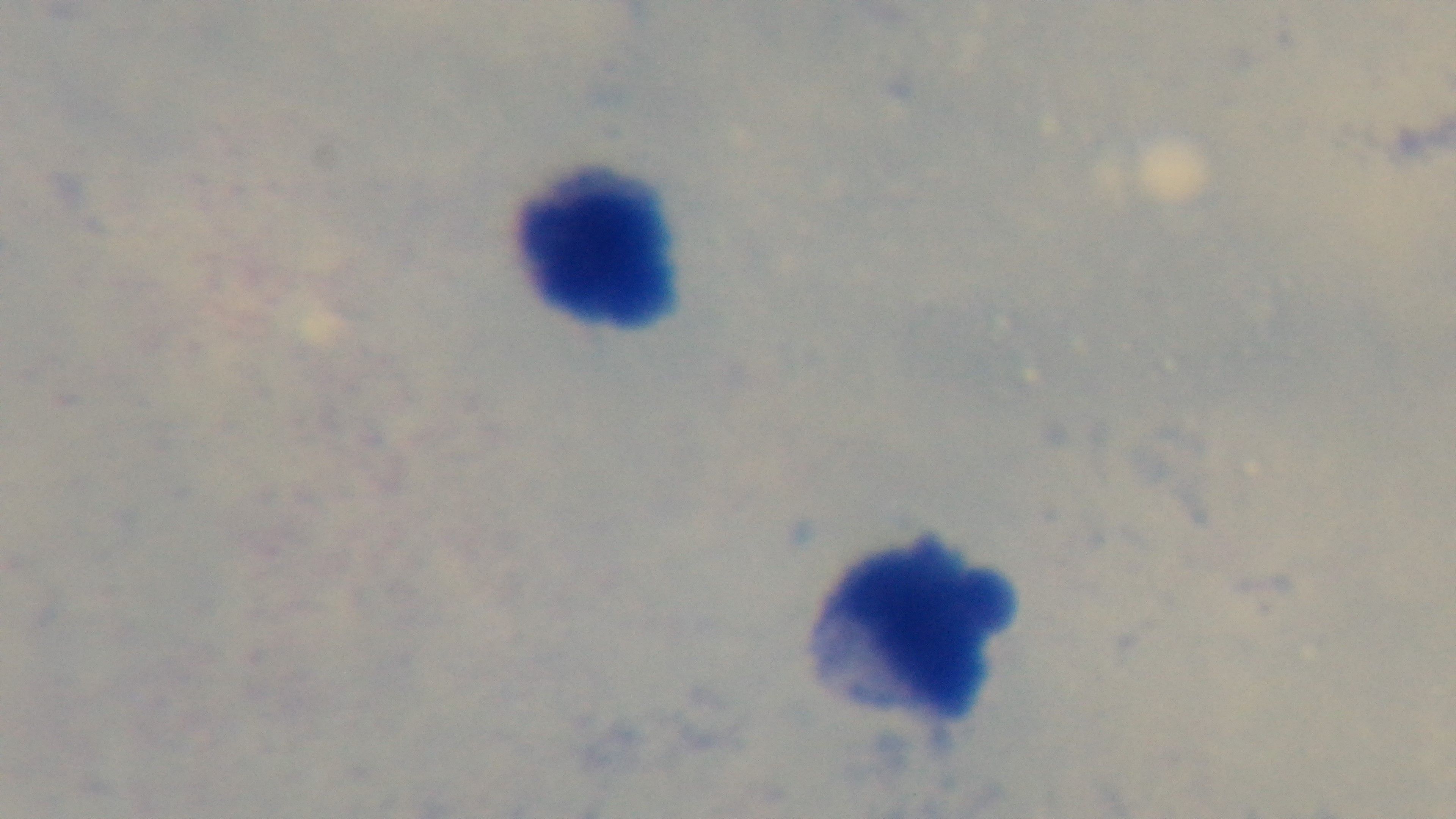
malaria_status: negative
field_of_view: single
capture: mounted 4K digital camera
stain: Giemsa
objective: 100x oil immersion
preparation: thick smear
modality: light microscopy